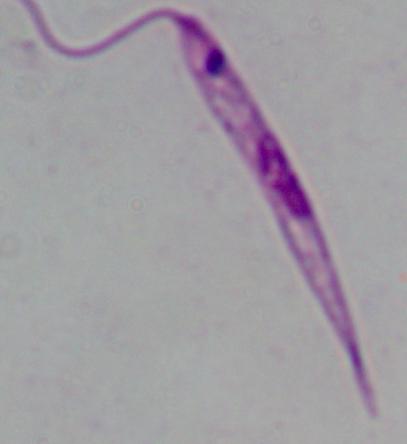

identification = Leishmania
magnification = 1000x
modality = micrograph